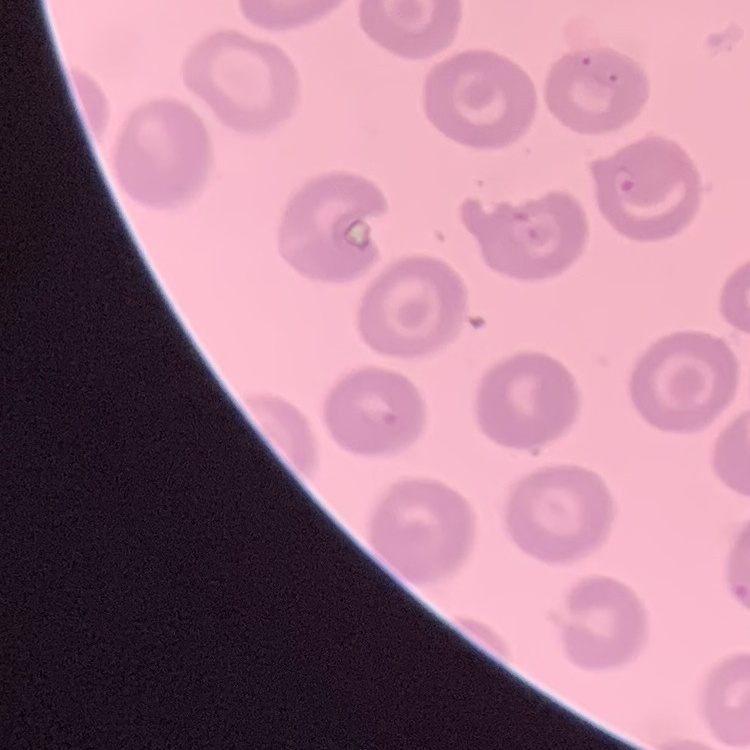
Summary:
  - Erythrocyte morphology: no rouleaux formation
  - Stain: Field's or Giemsa
  - Image type: one tile cut from a larger photomicrograph
  - Preparation: thin blood smear